Assess for parasitized red blood cells.
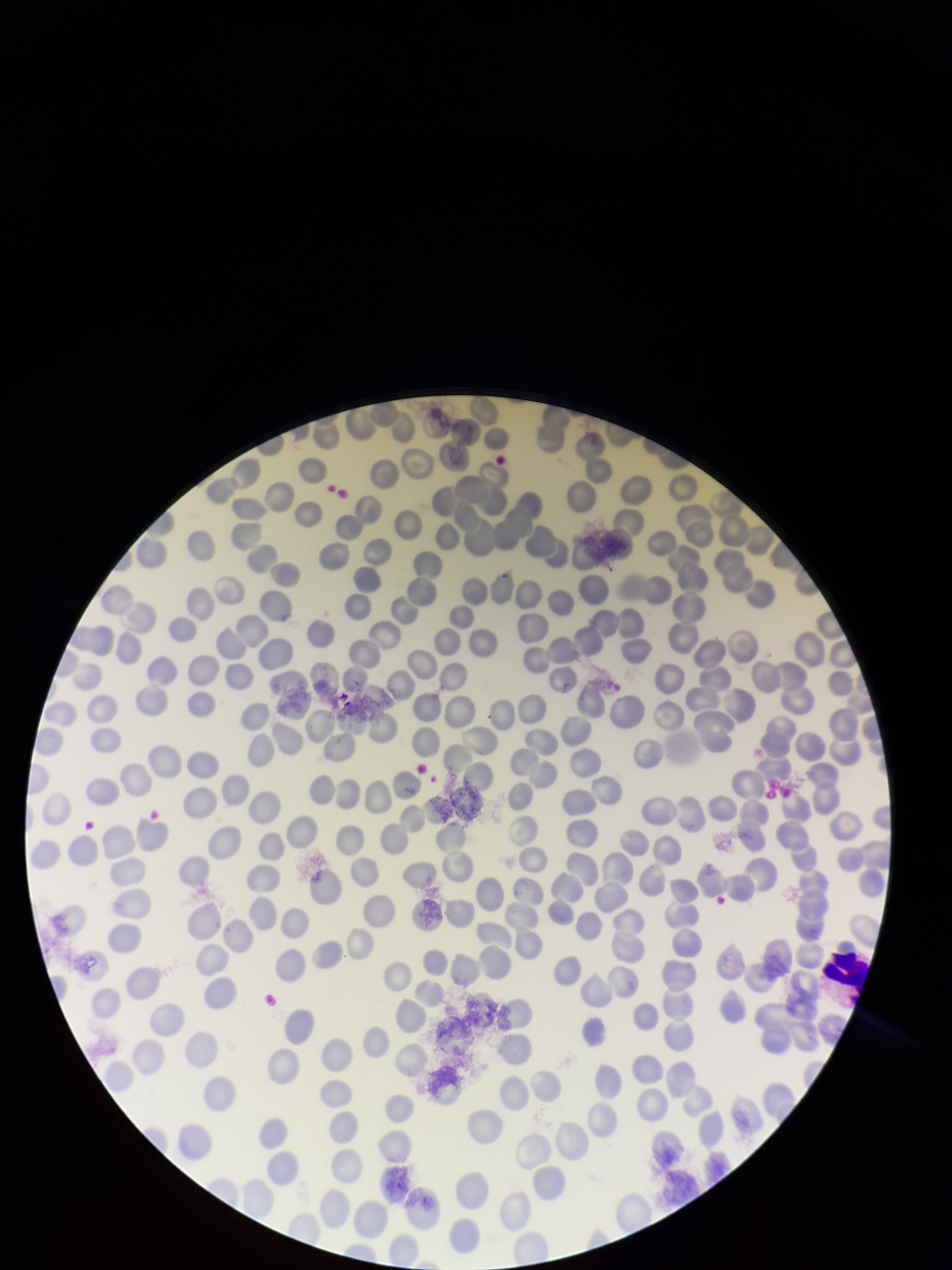

None detected.

field of view = one from this slide
preparation = thin blood smear
stain = Giemsa
capture = smartphone photograph through the microscope eyepiece
image size = 952×1270 pixels
red blood cell count = 244
parasitized red blood cell count = 0
patient malaria status = negative